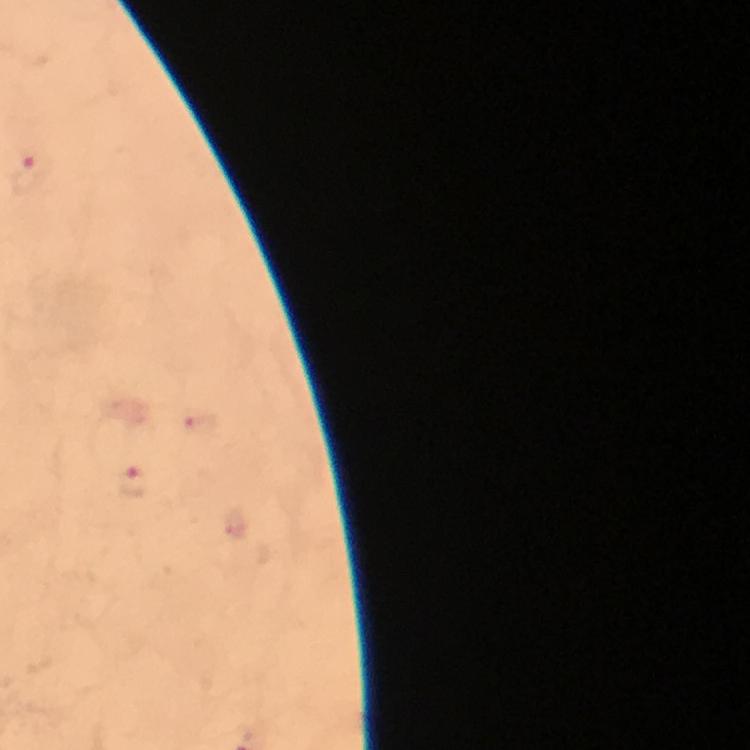 Approximate centers as [x, y] in pixels. Plasmodium parasite locations: [31, 174], [201, 423], [135, 481]. From a malaria diagnostic workup. Smartphone photograph taken through a microscope. Thick blood smear. Giemsa-stained preparation. Immersion oil was used. Cropped region of a single field of view. Image is 750×750 pixels. At 100x magnification.